Name the parasite shown.
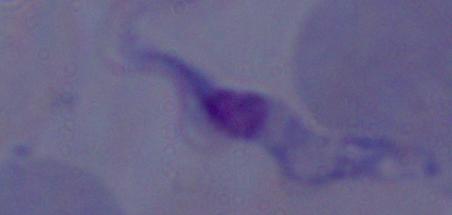
A trypanosome.

Summary:
  - Modality: photomicrograph
  - Magnification: 1000x